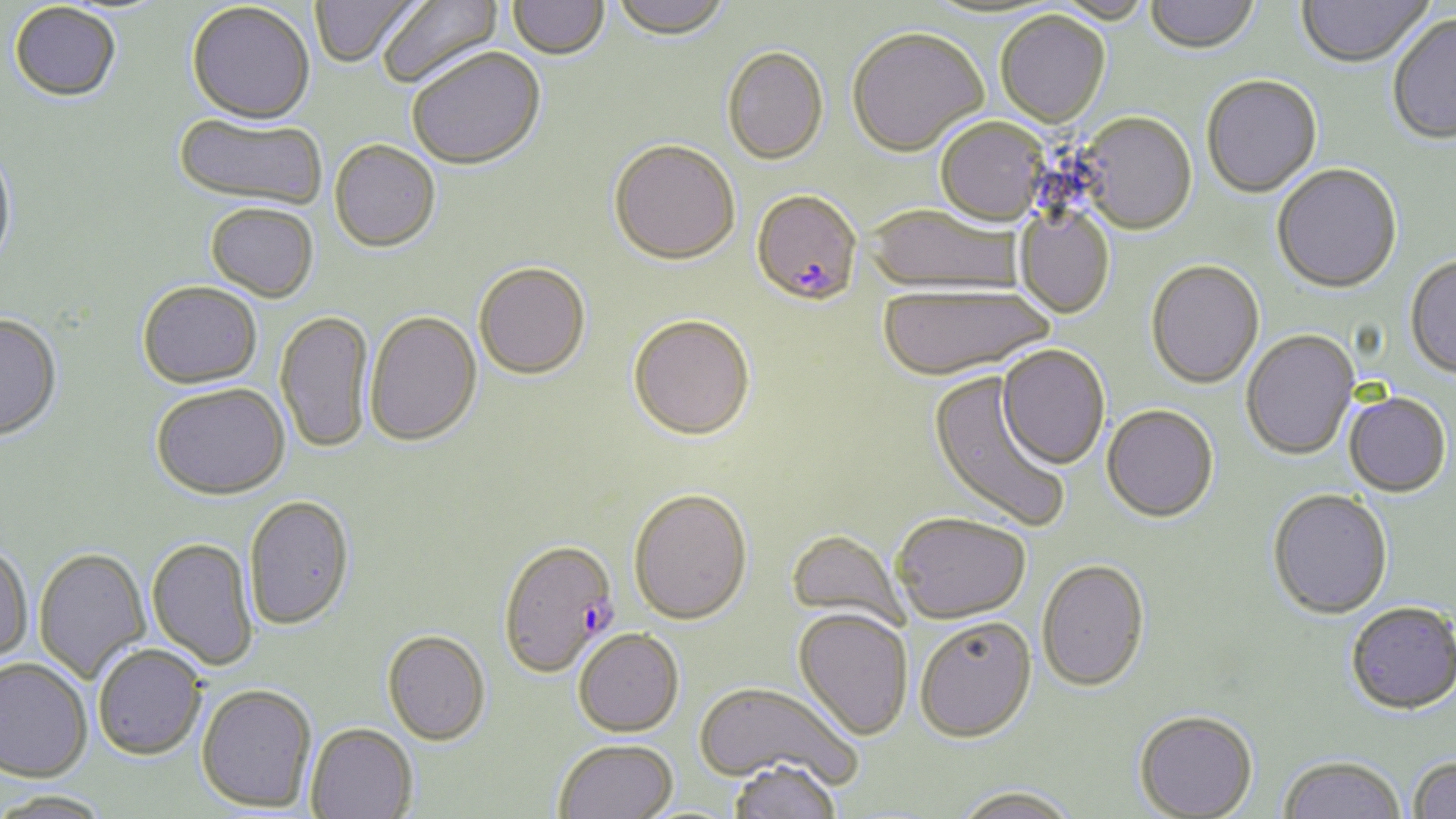

Approximate bounding boxes as (x1,y1)-(x2,y2) corner pairs in pixels. Plasmodium falciparum-infected red blood cell locations: (752,189)-(863,306), (497,537)-(619,678). Uninfected red blood cell locations: (309,0)-(424,68), (375,0)-(503,90), (610,0)-(733,39), (1048,0)-(1155,25), (1145,0)-(1259,55), (1297,0)-(1434,68), (508,1)-(609,60), (186,2)-(315,123), (9,3)-(122,102), (995,10)-(1111,127), (1387,14)-(1456,144), (846,26)-(988,156), (721,45)-(829,164), (406,46)-(546,169), (1201,74)-(1322,198), (1076,111)-(1197,234), (174,112)-(327,208), (935,117)-(1050,226), (608,138)-(740,263), (329,139)-(441,252), (0,141)-(18,274), (1272,163)-(1402,293), (205,202)-(319,301), (864,204)-(1022,293), (1014,205)-(1115,318), (1405,254)-(1456,380), (1146,259)-(1264,389), (473,261)-(591,379), (137,280)-(262,388), (877,283)-(1053,380), (275,309)-(373,453), (365,310)-(482,446), (628,313)-(755,439), (0,314)-(62,440), (1241,329)-(1360,460), (996,344)-(1110,470), (929,371)-(1072,533), (151,382)-(290,499), (1344,391)-(1451,497), (1102,404)-(1219,521), (627,487)-(753,625), (1267,488)-(1393,619), (243,494)-(355,629), (891,511)-(1031,622), (786,528)-(909,632), (146,536)-(259,670), (0,539)-(33,666), (34,546)-(151,684), (1037,557)-(1151,690), (1345,602)-(1456,716), (793,608)-(914,740), (914,615)-(1037,741), (573,628)-(684,736), (382,629)-(491,745), (92,644)-(207,760), (0,656)-(92,781), (693,679)-(863,790), (196,683)-(317,812), (1134,709)-(1259,818), (306,722)-(418,818), (553,738)-(679,819), (1407,755)-(1456,819), (1278,756)-(1406,819), (726,758)-(843,819), (951,784)-(1082,819), (1,790)-(113,818). Slide-level diagnosis: Plasmodium falciparum. Light microscopy. Image is 1456×819 pixels. May-Grünwald-Giemsa-stained preparation. One field of a larger specimen. Thin blood film. 1000x magnification.